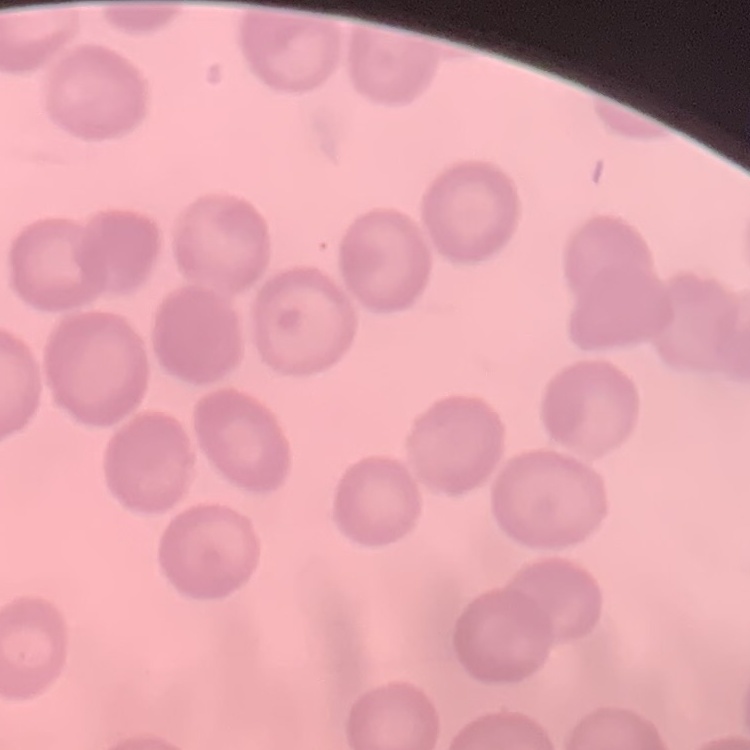
Summary:
  - Red blood cell morphology: no rouleaux formation
  - Image type: one tile cut from a larger photomicrograph
  - Preparation: thin peripheral smear
  - Stain: Field's or Giemsa